Outline each uninfected red blood cell.
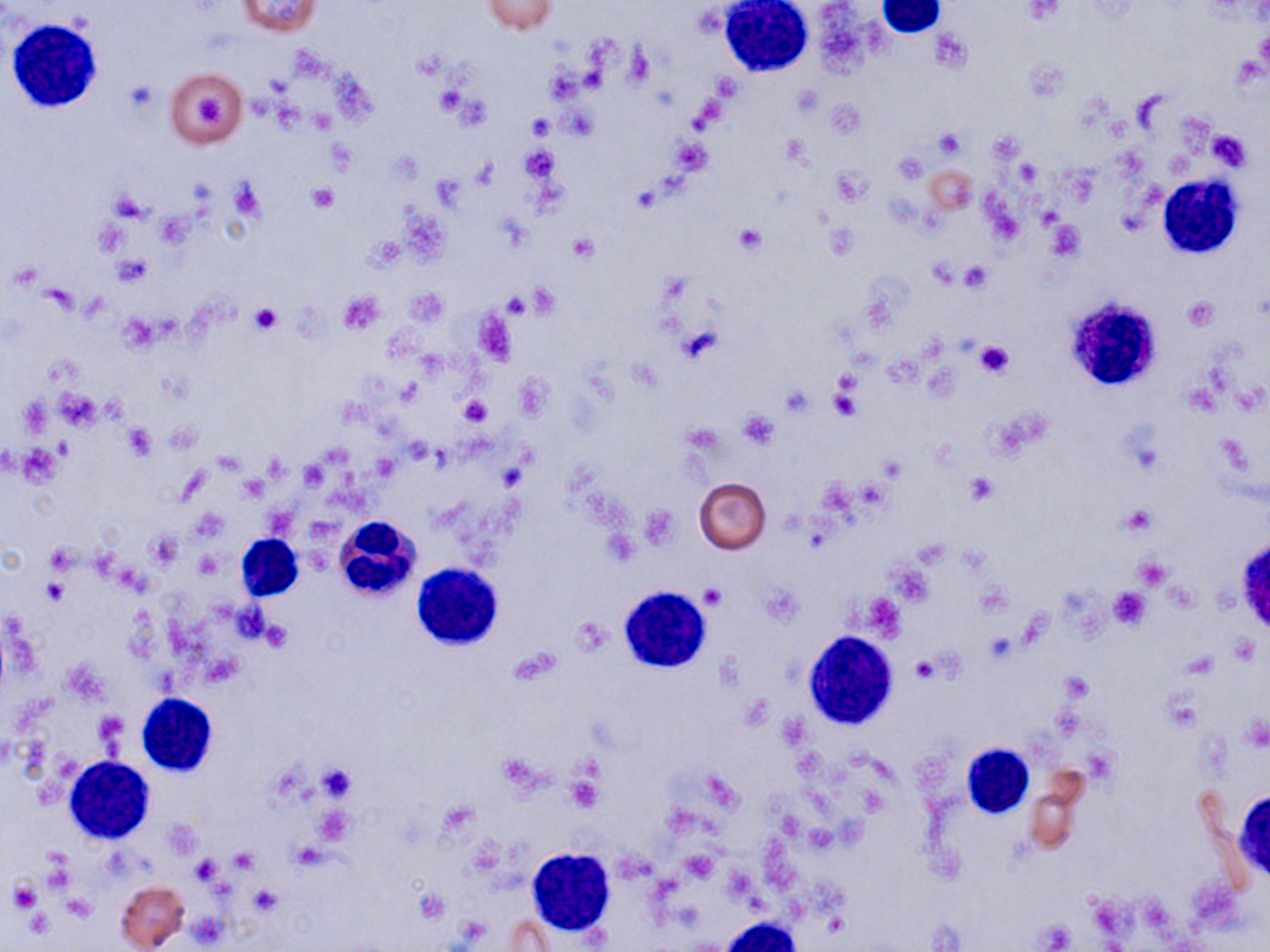

Approximate bounding boxes as (x1,y1)-(x2,y2) corner pairs in pixels.
Uninfected red blood cells: (235,0)-(321,36), (483,1)-(557,34), (167,67)-(247,148), (694,477)-(771,554), (1026,784)-(1079,855), (115,880)-(189,951), (503,915)-(560,949).

slide-level diagnosis = negative for blood parasites
modality = light microscopy
stain = May-Grünwald-Giemsa
white blood cell locations = approximate bounding boxes as (x1,y1)-(x2,y2) corner pairs in pixels: (719,1)-(814,78), (877,1)-(944,38), (8,19)-(104,111), (1158,175)-(1245,259), (1076,302)-(1157,391), (335,514)-(421,602), (236,533)-(304,601), (1238,540)-(1270,630), (415,560)-(506,655), (616,585)-(713,676), (802,632)-(899,729), (137,692)-(218,777), (961,745)-(1033,820), (64,755)-(156,843), (1241,794)-(1270,875), (527,846)-(617,936), (716,917)-(803,952)
magnification = 1000x
preparation = thin blood film
platelet locations = approximate bounding boxes as (x1,y1)-(x2,y2) corner pairs in pixels: (625,44)-(654,89), (546,69)-(582,103), (123,80)-(159,116), (434,86)-(468,119), (192,95)-(222,130), (562,105)-(597,139), (528,114)-(556,141), (935,130)-(965,159), (1208,131)-(1251,171), (326,138)-(358,175), (673,138)-(712,174), (519,144)-(560,182), (894,152)-(927,183), (229,178)-(267,221), (307,185)-(339,213), (112,192)-(151,221), (1048,221)-(1085,260), (734,225)-(765,255), (368,235)-(405,268), (568,235)-(598,263), (113,254)-(151,287), (959,261)-(991,291), (338,290)-(385,334), (503,292)-(531,317), (1183,297)-(1218,330), (250,304)-(283,335), (678,326)-(721,363), (974,340)-(1016,380), (778,385)-(816,416), (55,389)-(101,430), (829,390)-(863,423), (459,396)-(491,426), (21,397)-(51,436), (736,411)-(780,449), (121,423)-(156,460), (370,452)-(400,481), (301,461)-(327,488), (965,474)-(998,504), (264,502)-(296,538), (1120,505)-(1155,536), (145,530)-(181,570), (45,546)-(76,571), (196,552)-(223,577), (1134,557)-(1170,590), (42,578)-(69,605), (699,586)-(724,609), (1109,587)-(1152,629), (260,618)-(292,652), (911,655)-(940,683), (1059,671)-(1092,701), (316,763)-(357,801), (566,776)-(603,811), (228,847)-(258,875), (189,857)-(222,884), (8,881)-(41,912), (1037,922)-(1073,950)
image size = 1270×952 pixels
field of view = single